State which parasite is depicted.
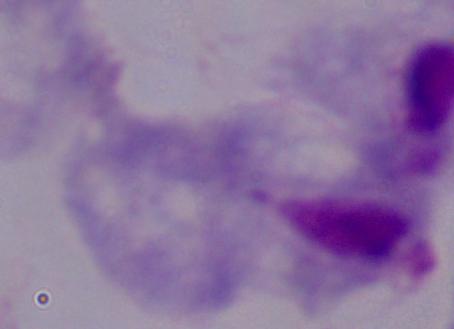
A trichomonad.

Summary:
  - Magnification: 1000x
  - Modality: photomicrograph